Report the malaria status of this cell.
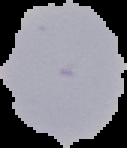
Uninfected.

image size = 127×148 pixels
preparation = thin blood smear
image type = segmented cell region on a black background